Evaluate for malaria.
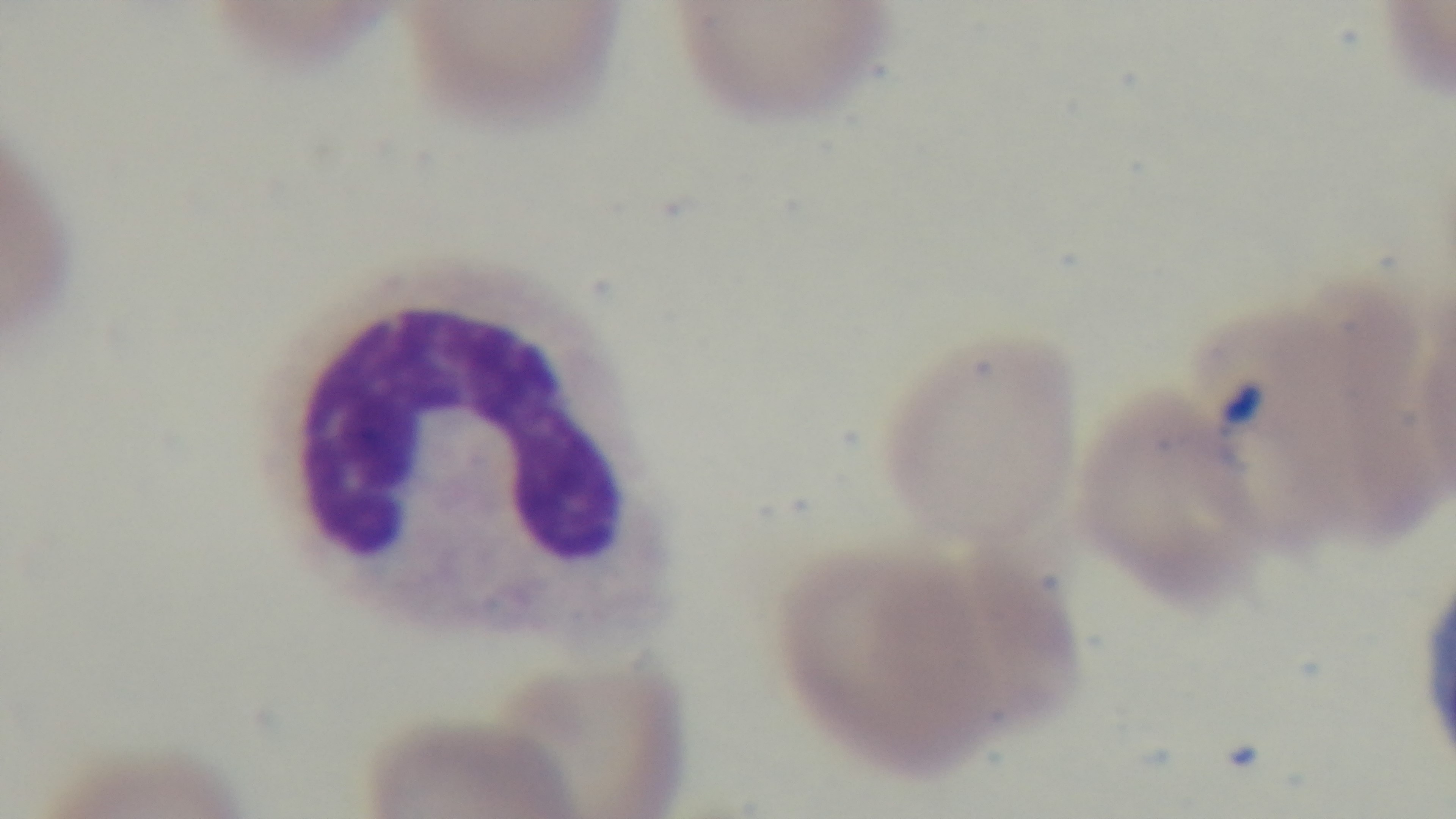
It is infected.

Photomicrograph. One field from the slide. Oil-immersion objective, 100x. Captured with a mounted 4K digital camera. Preparation: thin smear. Giemsa stain.